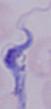

Photomicrograph. A trypanosome is shown. Captured at 1000x magnification.